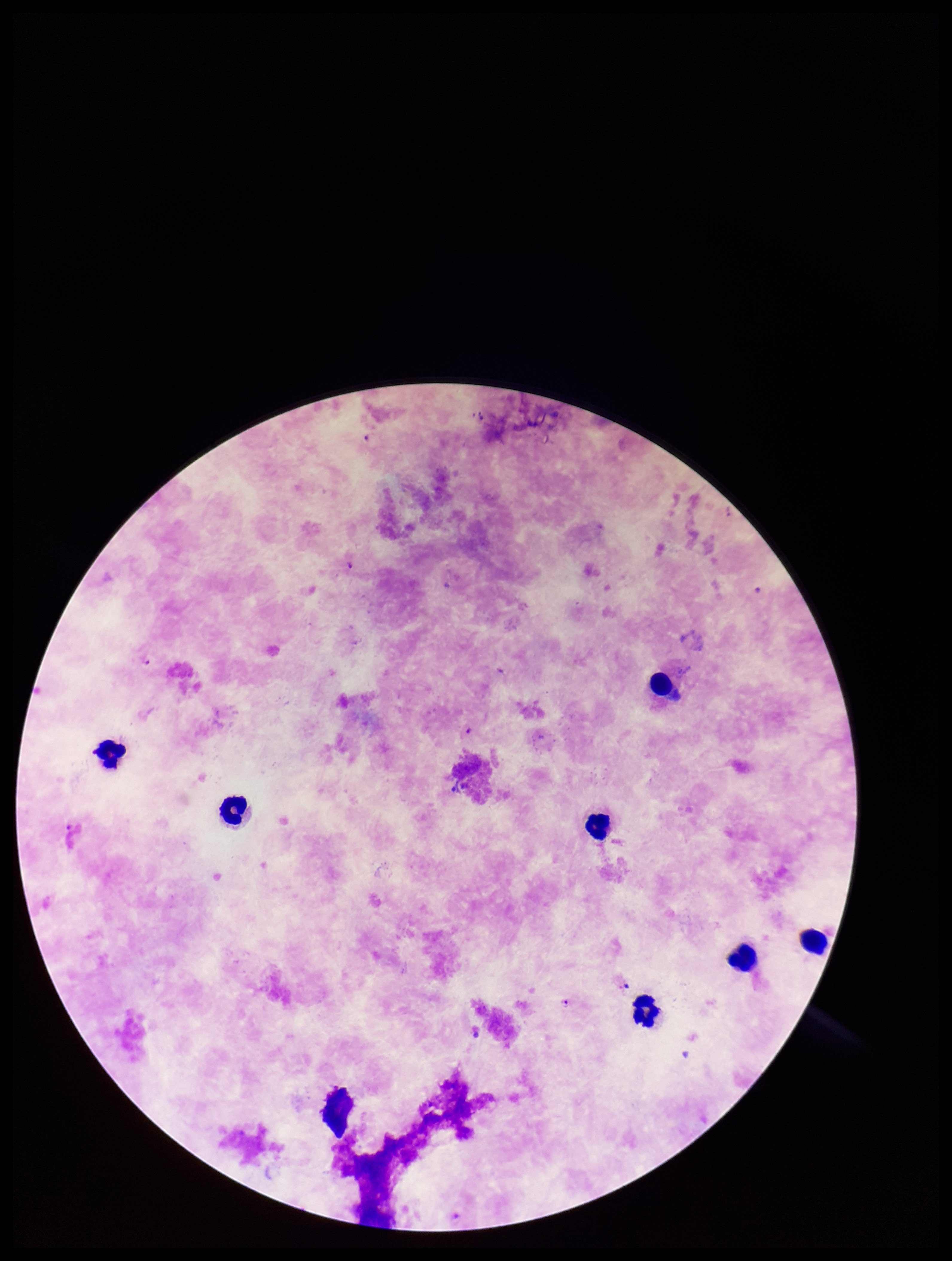
Summary:
  - Species reported for this patient: Plasmodium falciparum
  - Image size: 952×1261 pixels
  - Leukocyte count: 8
  - Plasmodium parasites: seen
  - Parasite count: 4
  - Stain: Giemsa
  - Field of view: single
  - Preparation: thick smear
  - Capture: smartphone photograph through the microscope eyepiece
  - Patient malaria status: infected